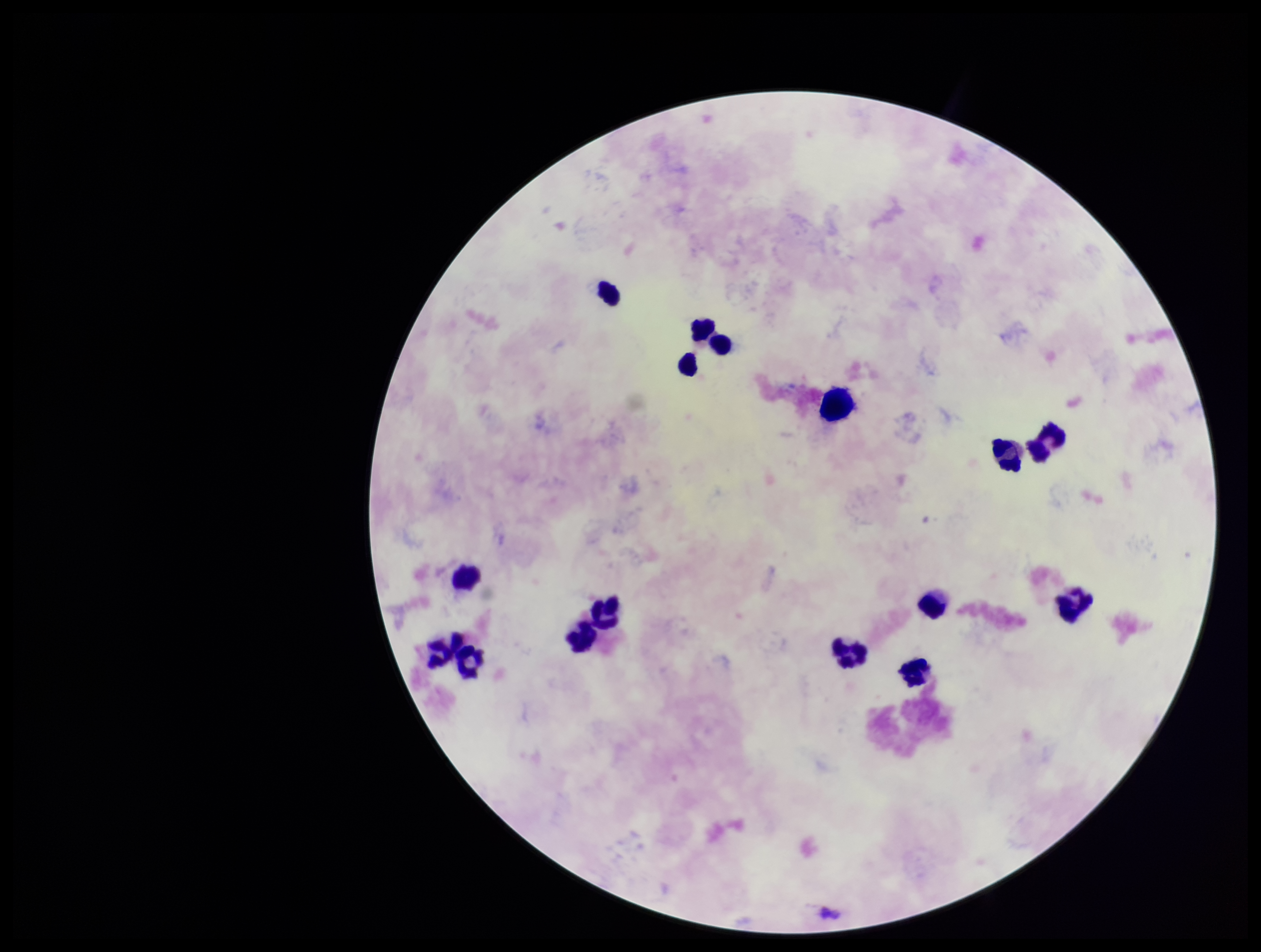

Summary:
  - Field of view: single
  - Patient malaria status: infected
  - Species reported for this patient: Plasmodium falciparum
  - Capture: smartphone photograph through the microscope eyepiece
  - Preparation: thick blood smear
  - Image size: 1261×952 pixels
  - Plasmodium parasites: none seen
  - Stain: Giemsa
  - Parasite count: 0
  - Leukocyte count: 16